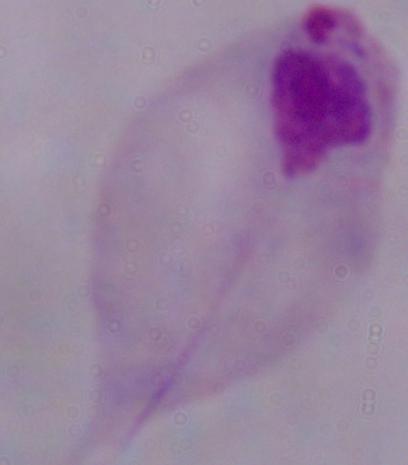

Captured at 1000x magnification. Photomicrograph. A trichomonad is shown.